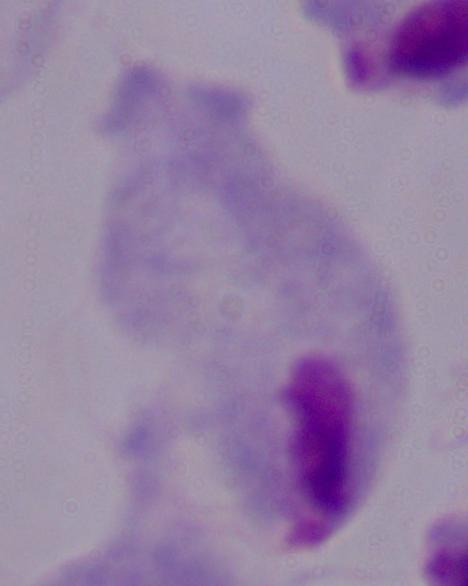

A trichomonad is shown. Photomicrograph. Captured at 1000x magnification.